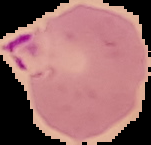 Cell region segmented out of the field of view; the surrounding area is masked to black. Image is 151×145 pixels. Malaria status: parasitized. From a thin blood smear.